Classify this cell by malaria status.
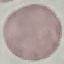

Uninfected.

Summary:
  - Image type: cell patch, automatically extracted from a larger field of view and resized to 64 × 64 pixels
  - Preparation: thin blood film
  - Capture: smartphone camera at the microscope eyepiece
  - Stain: Giemsa